Assess this cell for malaria.
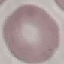

Uninfected.

Photographed with a smartphone camera at the microscope eyepiece. Giemsa-stained preparation. Thin smear of blood. Cell patch, automatically extracted from a larger field of view and resized to 64 × 64 pixels.